Assess this cell for malaria.
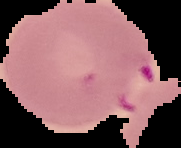

Parasitized.

Segmented cell region on a black background. Image is 181×148 pixels. From a thin blood film.